State which parasite is depicted.
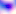
This is Toxoplasma gondii.

modality = photomicrograph
magnification = 400x